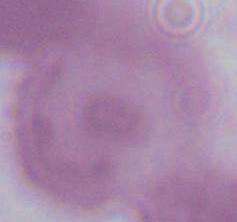

Summary:
  - Identification: red blood cell
  - Magnification: 1000x
  - Modality: photomicrograph